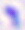 400x magnification. Photomicrograph. Toxoplasma gondii is shown.